Locate every blood parasite and identify its species.
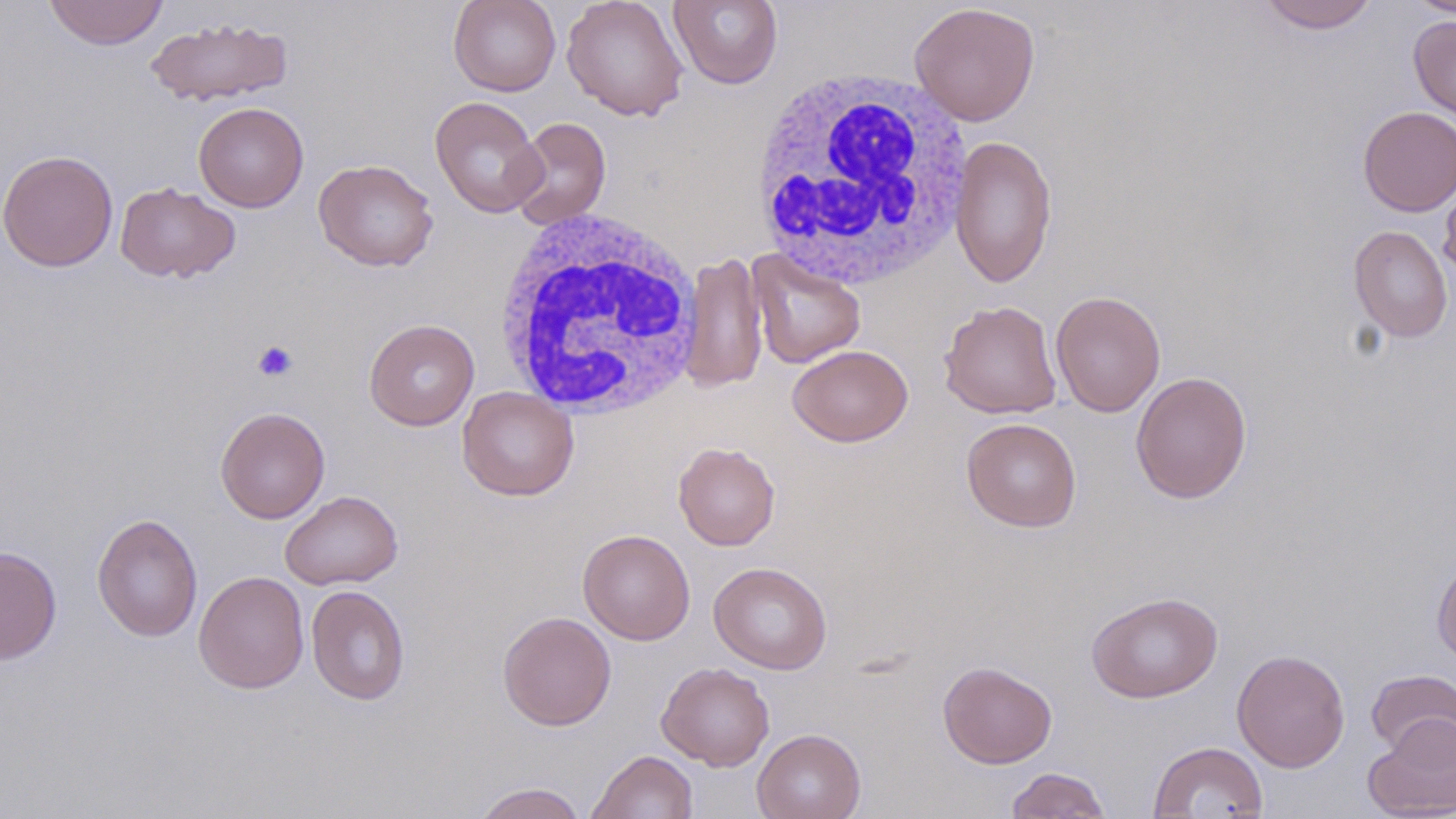

No blood parasites seen.

Summary:
  - Coordinate format: approximate bounding boxes as (x1,y1)-(x2,y2) corner pairs in pixels
  - Platelet locations: (251,339)-(299,381)
  - Uninfected red blood cell locations: (43,0)-(169,50), (448,0)-(562,96), (561,0)-(690,121), (668,0)-(784,90), (1408,0)-(1455,19), (1257,1)-(1379,33), (909,2)-(1040,126), (1408,15)-(1456,126), (144,17)-(294,107), (429,96)-(546,218), (193,102)-(309,212), (1358,106)-(1456,216), (507,116)-(611,230), (950,135)-(1058,289), (1,150)-(118,272), (313,158)-(439,272), (1439,169)-(1456,284), (115,182)-(240,283), (1348,224)-(1454,343), (747,249)-(867,369), (680,250)-(768,393), (1050,291)-(1166,418), (939,300)-(1062,419), (364,319)-(480,431), (787,344)-(913,447), (1131,371)-(1252,504), (457,387)-(580,501), (215,406)-(330,523), (961,417)-(1082,532), (673,442)-(780,550), (279,490)-(403,590), (91,513)-(203,642), (578,528)-(695,645), (0,546)-(62,664), (1432,555)-(1456,667), (708,561)-(832,674), (193,571)-(309,693), (306,585)-(410,705), (1086,591)-(1223,703), (497,611)-(616,731), (1232,649)-(1350,772), (938,661)-(1057,768), (656,662)-(775,770), (1365,668)-(1456,761), (1363,714)-(1456,818), (752,728)-(866,819), (1147,741)-(1269,818), (586,750)-(699,818), (1005,767)-(1112,818), (471,782)-(587,819)
  - White blood cell locations: (748,69)-(974,290), (491,208)-(704,418)
  - Slide-level diagnosis: no evidence of blood parasites
  - Image size: 1456×819 pixels
  - Preparation: thin blood film
  - Magnification: 1000x
  - Stain: May-Grünwald-Giemsa
  - Modality: light microscopy
  - Field of view: one of a larger specimen